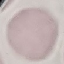

Malaria status: uninfected. Automatically extracted cell patch, resized to 64 × 64 pixels. Acquired by smartphone through the microscope eyepiece. Giemsa-stained preparation. Thin smear of blood.